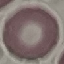

malaria_status: uninfected
stain: Giemsa
image_type: cell patch, automatically extracted from a larger field of view and resized to 64 × 64 pixels
capture: smartphone camera at the microscope eyepiece
preparation: thin blood film